Classify this cell by malaria status.
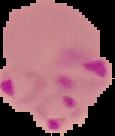
It is parasitized.

preparation = thin blood film
image type = segmented cell region with the area outside set to black
image size = 115×136 pixels